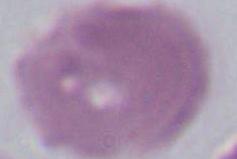
Summary:
  - Magnification: 1000x
  - Identification: erythrocyte
  - Modality: micrograph